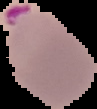

Summary:
  - Preparation: thin blood smear
  - Image size: 97×109 pixels
  - Malaria status: parasitized
  - Image type: cell region segmented out of the field of view; surrounding area masked to black